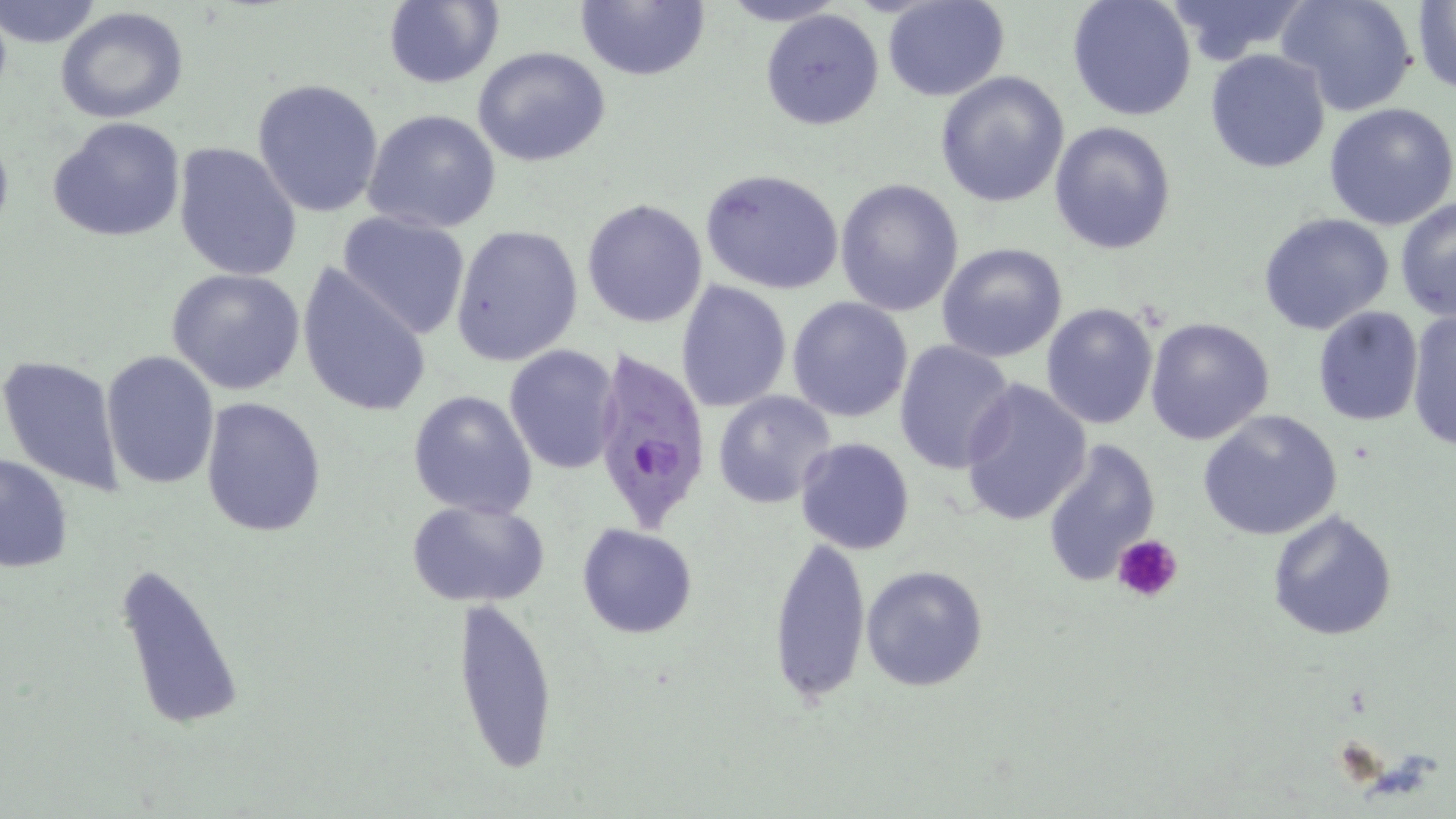 Approximate bounding boxes as [x1, y1, x2, y2] in pixels. Plasmodium falciparum-infected red blood cell locations: [587, 347, 714, 533]. Uninfected red blood cell locations: [1, 0, 104, 49], [382, 0, 503, 88], [575, 0, 710, 83], [882, 0, 1009, 101], [1067, 0, 1198, 122], [1161, 0, 1313, 66], [1278, 0, 1419, 117], [1411, 2, 1456, 96], [55, 7, 191, 125], [760, 8, 886, 131], [472, 46, 613, 168], [1204, 49, 1331, 173], [934, 71, 1070, 208], [252, 77, 385, 218], [1324, 101, 1456, 230], [362, 108, 502, 234], [48, 116, 188, 243], [1049, 122, 1176, 255], [172, 142, 303, 282], [699, 167, 847, 297], [834, 179, 965, 319], [582, 198, 709, 329], [1395, 198, 1455, 321], [335, 211, 473, 341], [1259, 212, 1394, 336], [450, 223, 584, 366], [935, 242, 1069, 361], [298, 265, 433, 419], [167, 267, 308, 395], [676, 281, 792, 412], [786, 297, 914, 422], [1041, 303, 1159, 429], [1311, 305, 1426, 425], [1408, 309, 1455, 453], [1144, 316, 1276, 444], [894, 340, 1019, 473], [504, 345, 621, 474], [100, 350, 219, 490], [0, 353, 126, 494], [959, 379, 1093, 527], [407, 389, 539, 518], [711, 389, 837, 508], [201, 398, 327, 539], [1198, 409, 1343, 541], [794, 436, 917, 555], [1042, 436, 1161, 589], [1, 453, 74, 573], [406, 497, 552, 609], [1265, 510, 1397, 643], [577, 522, 700, 639], [768, 532, 871, 707], [108, 556, 247, 737], [860, 564, 989, 692], [449, 595, 559, 776]. Platelet locations: [1114, 534, 1185, 605]. Slide-level diagnosis: Plasmodium falciparum. Thin blood film. Captured at 1000x magnification. Single field of view. May-Grünwald-Giemsa stain. Optical microscopy. Image is 1456×819 pixels.